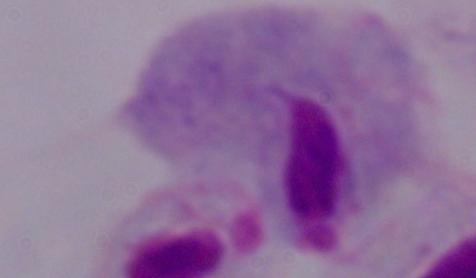
magnification = 1000x
modality = micrograph
identification = trichomonad